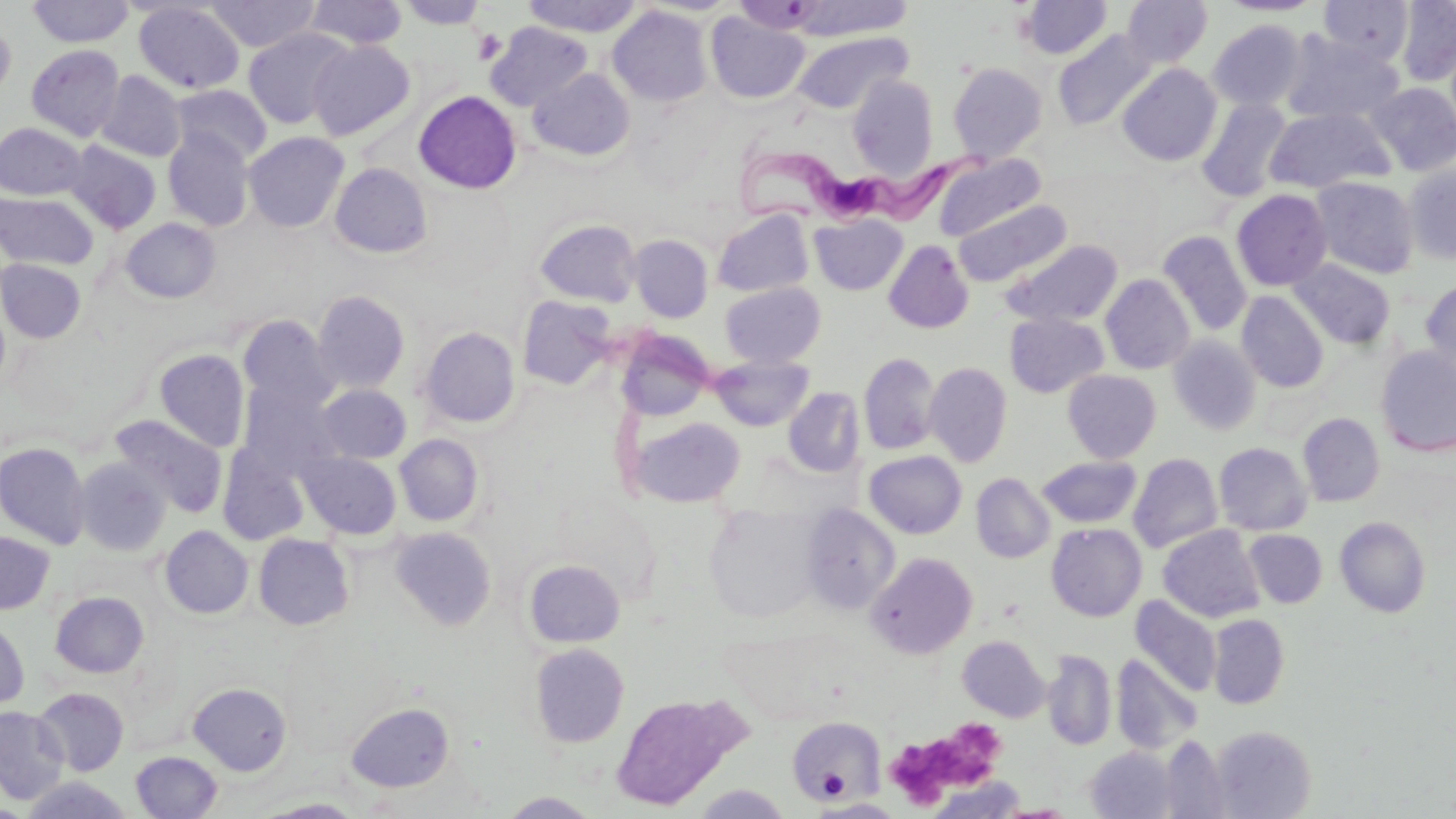

{
  "slide_level_diagnosis": "Trypanosoma brucei",
  "uninfected_red_blood_cell_locations": "approximate bounding boxes as [x1, y1, x2, y2] in pixels: [204, 0, 321, 52], [304, 0, 408, 49], [520, 0, 644, 37], [792, 0, 913, 40], [1019, 0, 1112, 59], [1121, 0, 1212, 68], [1218, 0, 1324, 16], [1319, 0, 1414, 66], [1396, 0, 1456, 85], [27, 1, 134, 47], [398, 1, 487, 29], [133, 2, 245, 93], [607, 6, 712, 107], [705, 12, 810, 104], [0, 19, 16, 100], [1208, 20, 1307, 111], [485, 22, 592, 111], [243, 28, 354, 129], [1053, 30, 1156, 131], [791, 31, 912, 114], [1282, 33, 1402, 125], [308, 39, 415, 140], [26, 44, 125, 141], [947, 62, 1048, 163], [1117, 64, 1222, 166], [528, 68, 635, 161], [96, 70, 187, 162], [848, 73, 939, 179], [1367, 82, 1456, 175], [171, 84, 272, 165], [413, 90, 522, 194], [1197, 99, 1292, 202], [1265, 107, 1394, 193], [0, 122, 86, 200], [162, 128, 256, 231], [243, 131, 349, 232], [65, 140, 161, 233], [935, 154, 1045, 242], [330, 162, 432, 258], [1403, 163, 1456, 265], [1313, 178, 1420, 278], [1231, 189, 1332, 291], [0, 191, 98, 270], [953, 199, 1071, 287], [712, 210, 814, 297], [810, 214, 908, 295], [120, 217, 221, 303], [535, 219, 642, 307], [1158, 230, 1252, 337], [628, 234, 713, 322], [1000, 239, 1123, 329], [883, 240, 974, 333], [0, 258, 86, 343], [1289, 258, 1395, 349], [1101, 274, 1195, 374], [1420, 278, 1456, 374], [720, 282, 825, 368], [312, 290, 410, 394], [1237, 291, 1329, 392], [517, 295, 618, 390], [1004, 313, 1109, 398], [238, 314, 340, 414], [419, 326, 520, 428], [616, 331, 713, 421], [1168, 336, 1261, 436], [1375, 347, 1456, 457], [154, 348, 250, 452], [859, 352, 940, 454], [711, 356, 814, 431], [924, 362, 1013, 467], [1063, 369, 1161, 463], [238, 383, 342, 478], [316, 384, 411, 463], [783, 387, 865, 477], [1298, 412, 1385, 507], [110, 414, 227, 517], [626, 414, 746, 508], [394, 434, 483, 526], [0, 441, 92, 549], [1214, 442, 1312, 535], [218, 443, 311, 547], [298, 450, 401, 539], [864, 451, 967, 538], [1128, 452, 1223, 554], [74, 456, 172, 556], [1037, 456, 1142, 528], [971, 473, 1055, 563], [800, 504, 899, 615], [704, 506, 820, 622], [1335, 516, 1431, 618], [1046, 522, 1147, 621], [160, 525, 253, 619], [1158, 525, 1265, 623], [391, 526, 496, 631], [1244, 529, 1327, 608], [0, 531, 55, 615], [253, 533, 354, 630], [867, 552, 978, 658], [524, 558, 624, 648], [50, 591, 149, 677], [1131, 596, 1221, 697], [1209, 614, 1290, 709], [0, 617, 30, 710], [957, 635, 1050, 721], [530, 643, 630, 747], [1043, 648, 1116, 751], [1111, 654, 1202, 755], [188, 681, 292, 775], [33, 686, 129, 775], [610, 693, 746, 811], [346, 701, 455, 791], [0, 706, 70, 805], [787, 717, 886, 802], [1211, 725, 1318, 818], [1158, 735, 1232, 819], [1086, 746, 1178, 819], [130, 751, 222, 818], [927, 777, 1029, 818], [692, 785, 792, 818], [501, 791, 601, 818], [258, 798, 366, 818], [812, 799, 905, 817], [994, 803, 1076, 818]",
  "stain": "May-Grünwald-Giemsa",
  "image_size": "1456×819 pixels",
  "platelet_locations": "approximate bounding boxes as [x1, y1, x2, y2] in pixels: [472, 29, 507, 65], [896, 722, 1001, 806], [817, 771, 849, 801]",
  "trypanosoma_brucei_locations": "approximate bounding boxes as [x1, y1, x2, y2] in pixels: [733, 137, 996, 223]",
  "preparation": "thin blood smear",
  "modality": "optical microscopy",
  "field_of_view": "single",
  "magnification": "1000x"
}